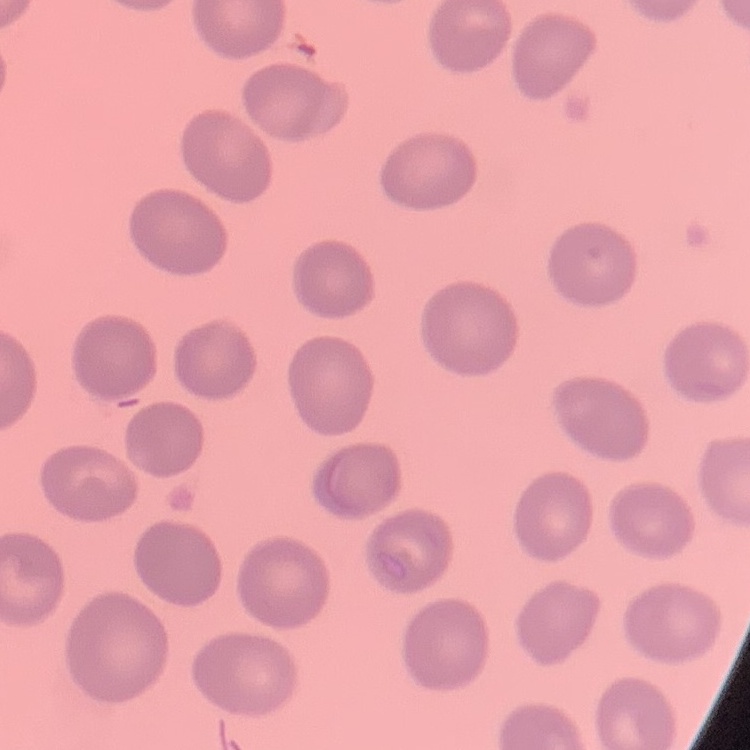

Summary:
  - Erythrocyte morphology: no rouleaux formation
  - Stain: Field's or Giemsa
  - Image type: one tile cut from a larger photomicrograph
  - Preparation: thin blood film